Assess for Plasmodium parasites.
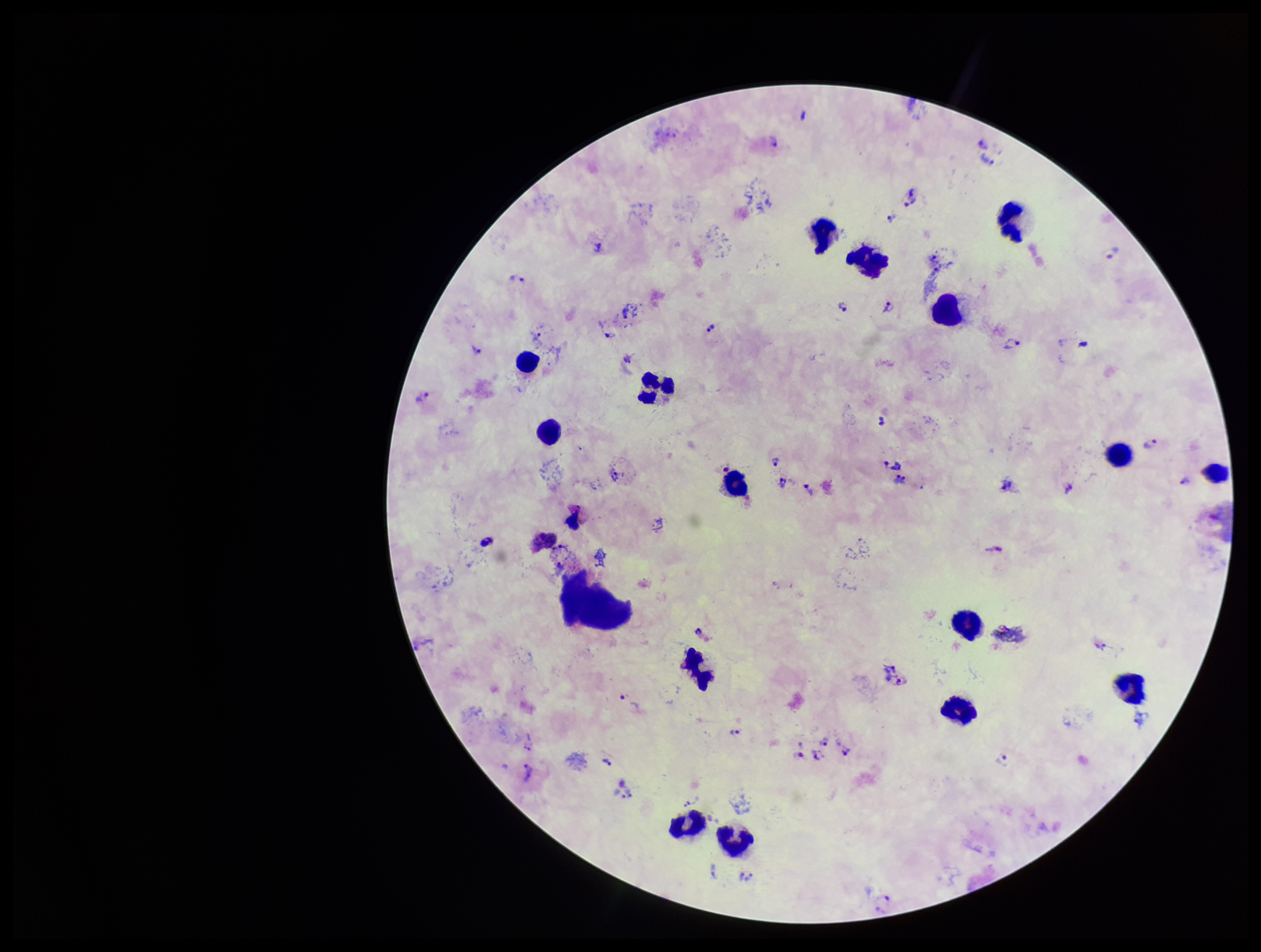
Identified.

Summary:
  - Image size: 1261×952 pixels
  - Patient malaria status: infected
  - Leukocyte count: 16
  - Parasite count: 37
  - Species reported for this patient: Plasmodium vivax
  - Stain: Giemsa
  - Preparation: thick blood smear
  - Field of view: single
  - Capture: smartphone photograph through the microscope eyepiece